State which cell type is depicted.
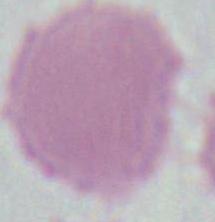
An erythrocyte.

Summary:
  - Magnification: 1000x
  - Modality: photomicrograph